Assess this cell for malaria.
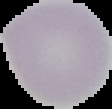

It is uninfected.

Image is 112×109 pixels. Cell region segmented out of the field of view; the surrounding area is masked to black. From a thin blood smear.